Locate every blood parasite and identify its species.
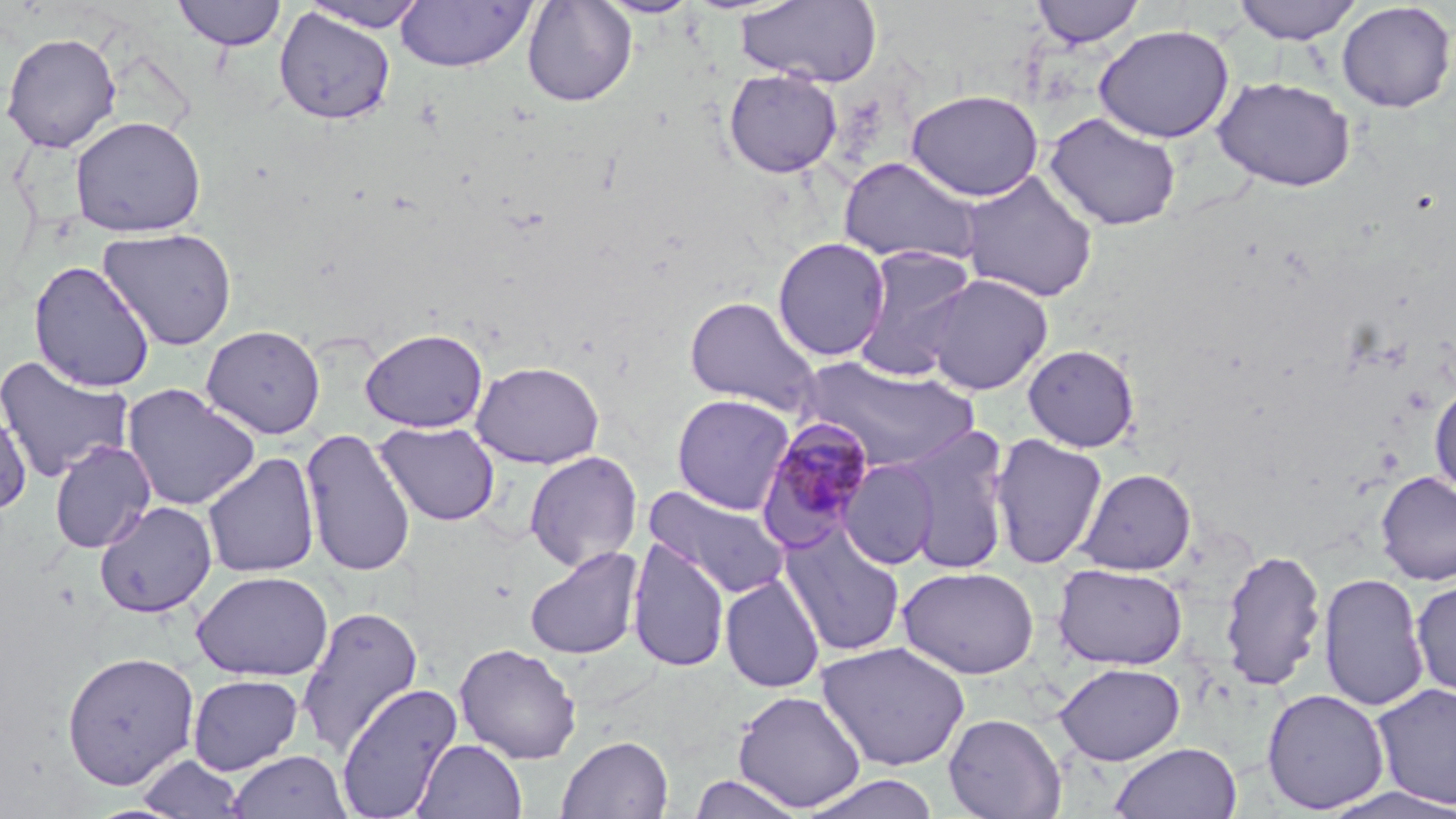
Approximate bounding boxes as [x1, y1, x2, y2] in pixels.
Plasmodium malariae-infected red blood cells: [756, 418, 878, 548].
No Plasmodium falciparum, Plasmodium ovale, Plasmodium vivax, Babesia divergens, or Trypanosoma brucei observed.

slide-level diagnosis = Plasmodium malariae
image size = 1456×819 pixels
stain = May-Grünwald-Giemsa
modality = optical microscopy
field of view = single
magnification = 1000x
uninfected red blood cell locations = approximate bounding boxes as [x1, y1, x2, y2] in pixels: [172, 0, 288, 51], [298, 0, 430, 32], [522, 0, 637, 107], [594, 0, 703, 18], [737, 0, 883, 87], [1029, 0, 1146, 48], [1230, 0, 1363, 44], [395, 1, 535, 72], [1336, 2, 1456, 113], [274, 7, 396, 125], [1093, 24, 1235, 144], [1, 31, 122, 153], [723, 69, 843, 178], [1212, 75, 1357, 192], [905, 89, 1044, 201], [1043, 112, 1182, 232], [70, 115, 206, 237], [837, 156, 982, 266], [958, 170, 1099, 303], [97, 227, 238, 350], [772, 237, 891, 361], [853, 246, 979, 381], [28, 260, 156, 393], [923, 272, 1053, 396], [684, 294, 822, 415], [201, 324, 326, 439], [359, 327, 489, 433], [1022, 344, 1140, 452], [0, 355, 134, 483], [795, 356, 981, 473], [471, 360, 604, 469], [1429, 382, 1456, 497], [122, 383, 261, 511], [671, 393, 795, 513], [0, 399, 33, 516], [374, 421, 500, 527], [893, 427, 1013, 575], [299, 428, 417, 577], [989, 433, 1108, 570], [49, 440, 156, 553], [524, 450, 642, 572], [201, 452, 320, 578], [838, 458, 939, 569], [1076, 468, 1196, 576], [1374, 471, 1456, 586], [643, 484, 792, 600], [94, 500, 218, 617], [780, 524, 906, 657], [627, 538, 730, 673], [524, 546, 644, 660], [1218, 547, 1328, 693], [1052, 563, 1188, 670], [898, 566, 1039, 679], [192, 570, 334, 681], [1318, 572, 1429, 711], [719, 573, 825, 693], [1411, 578, 1456, 700], [297, 605, 423, 756], [816, 641, 970, 772], [454, 642, 582, 764], [61, 650, 200, 790], [1054, 662, 1185, 765], [188, 674, 304, 774], [335, 682, 463, 818], [1370, 682, 1456, 811], [1261, 688, 1390, 814], [732, 689, 867, 812], [943, 713, 1067, 819], [556, 734, 673, 818], [414, 739, 527, 819], [1109, 742, 1242, 819], [227, 750, 351, 819], [137, 753, 246, 818], [689, 773, 806, 818], [799, 773, 941, 819]
preparation = thin blood film